Report the malaria status of this cell.
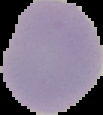
It is uninfected.

From a thin blood smear. Image is 103×115 pixels. Segmented cell region on a black background.